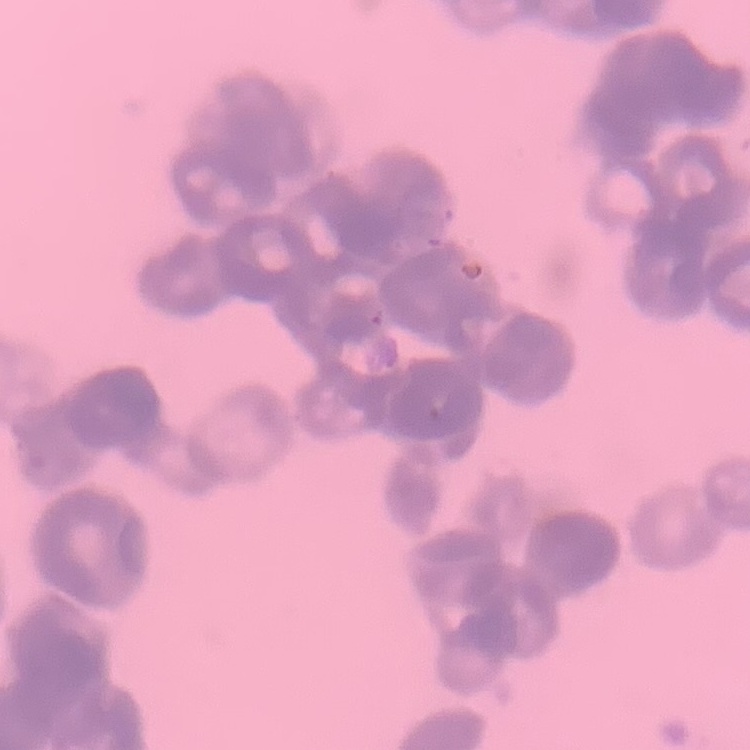

Summary:
  - Erythrocyte morphology: rouleaux formation
  - Stain: Field's or Giemsa
  - Image type: one tile cut from a larger photomicrograph
  - Preparation: thin blood film